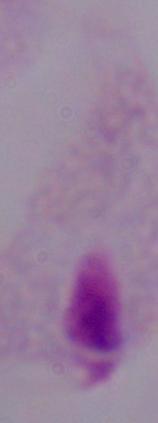

Summary:
  - Identification: trichomonad
  - Modality: photomicrograph
  - Magnification: 1000x